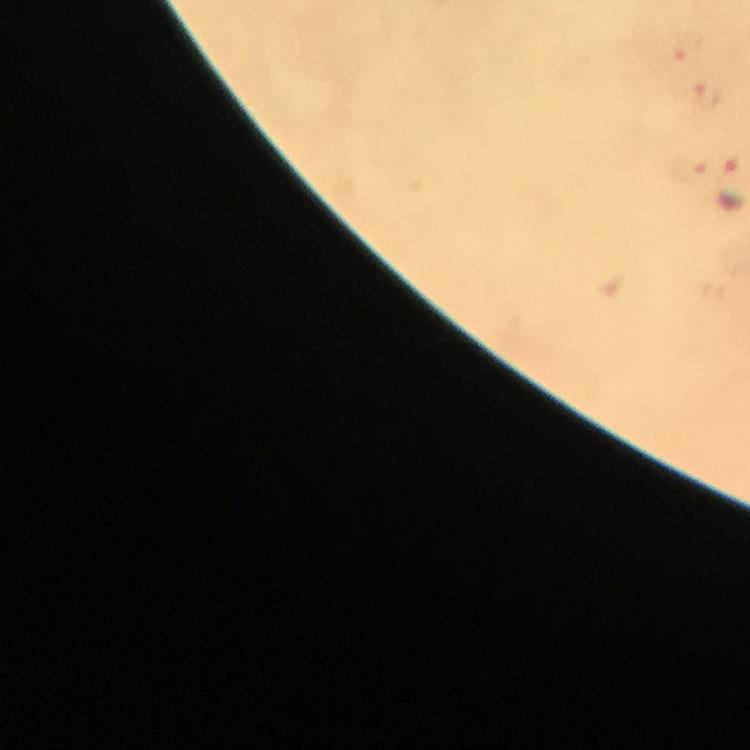

Approximate object centers, in pixels from the top-left corner. Malaria parasite locations: (x=689, y=48), (x=706, y=93). From a diagnostic examination for malaria. Thick blood smear. Giemsa-stained preparation. Cropped region of a single field of view. At 100x magnification. Immersion oil applied. Photographed with a smartphone mounted on the microscope. Image is 750×750 pixels.